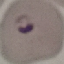
Malaria status: parasitized. Giemsa-stained preparation. Acquired by smartphone through the microscope eyepiece. Thin blood film. Automatically extracted cell patch, resized to 64 × 64 pixels.